Report the malaria status of this cell.
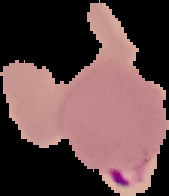
Parasitized.

preparation: thin blood smear
image_size: 169×196 pixels
image_type: cell region segmented out of the field of view; surrounding area masked to black